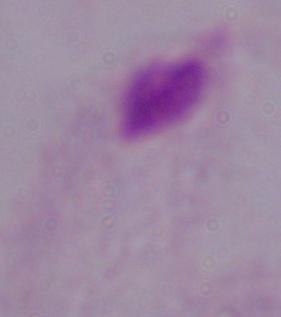

Micrograph. A trichomonad is seen. 1000x magnification.